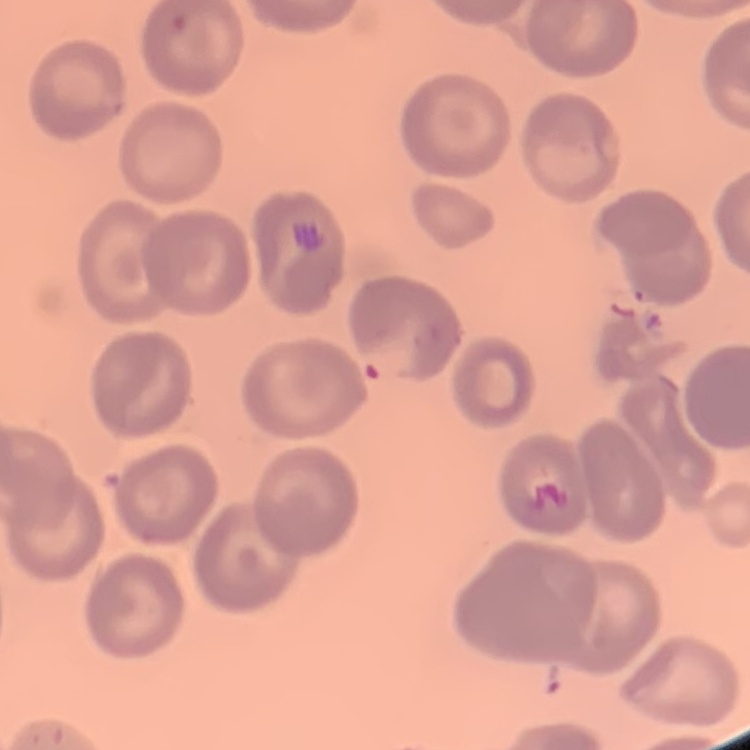

The red blood cells show no rouleaux formation. Field's or Giemsa stain. Thin blood smear. One tile cut from a larger photomicrograph.